Locate and identify every blood parasite.
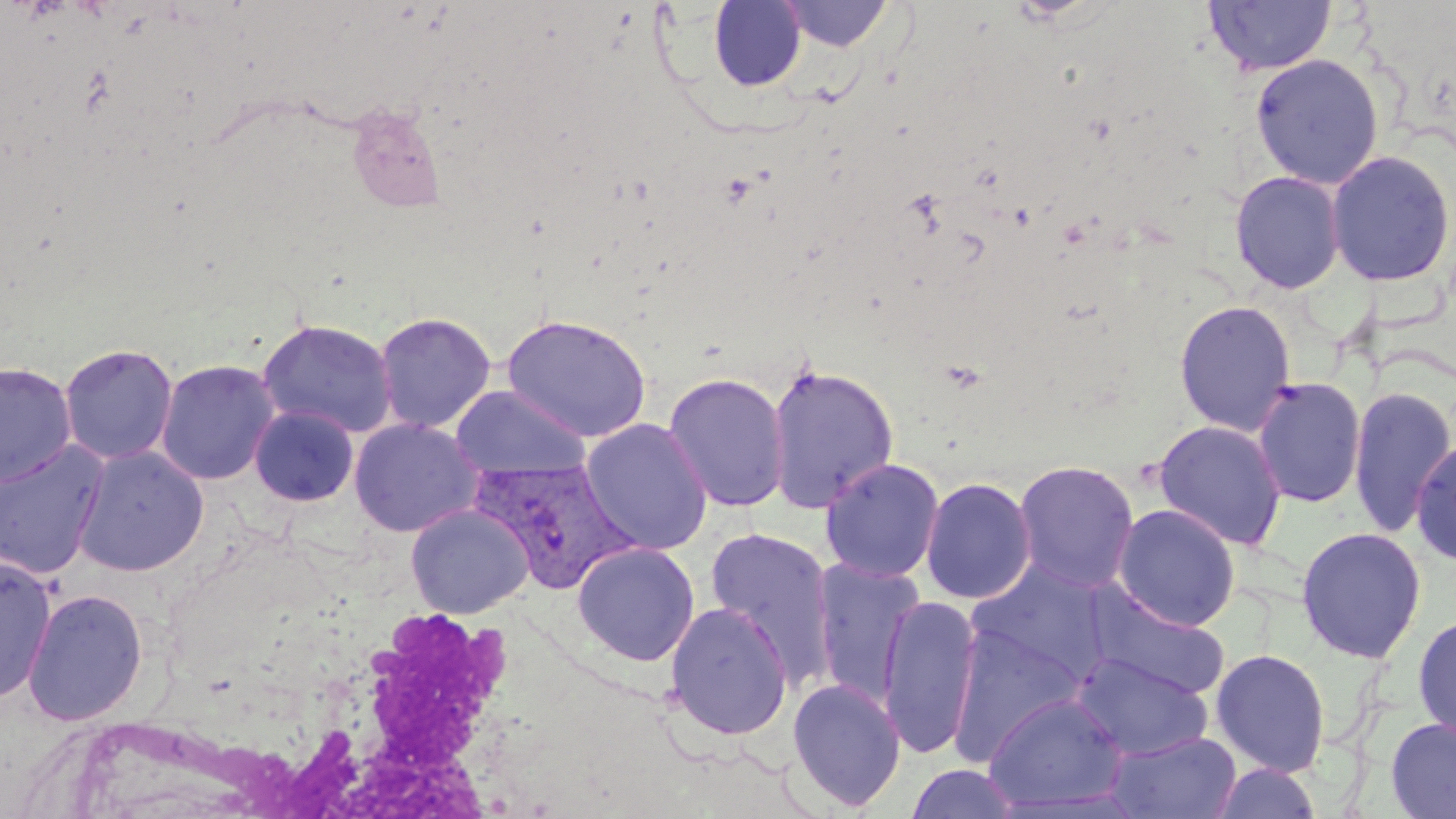

Approximate bounding boxes as (x1, y1, x2, y2) in pixels.
Plasmodium vivax-infected red blood cells: (469, 457, 639, 595).
No Plasmodium falciparum, Plasmodium ovale, Plasmodium malariae, Babesia divergens, or Trypanosoma brucei observed.

Summary:
  - Uninfected red blood cell locations: (1204, 0, 1336, 77), (709, 1, 806, 91), (779, 1, 894, 52), (1250, 53, 1385, 189), (346, 104, 447, 215), (1325, 149, 1455, 288), (1229, 170, 1346, 294), (1174, 300, 1296, 436), (374, 311, 496, 433), (501, 313, 652, 441), (257, 318, 398, 438), (59, 343, 178, 466), (156, 359, 281, 485), (0, 361, 76, 487), (764, 362, 899, 513), (663, 372, 791, 512), (1252, 376, 1366, 508), (450, 385, 592, 481), (1348, 385, 1456, 538), (249, 405, 360, 507), (580, 417, 713, 556), (348, 418, 485, 537), (1152, 419, 1288, 551), (1411, 438, 1456, 566), (0, 440, 110, 579), (72, 445, 209, 576), (819, 457, 944, 582), (1012, 459, 1140, 593), (920, 476, 1036, 604), (1112, 503, 1241, 631), (405, 504, 534, 618), (1295, 526, 1427, 663), (704, 527, 838, 686), (572, 541, 700, 665), (0, 555, 58, 702), (812, 559, 924, 707), (966, 559, 1112, 687), (1084, 585, 1231, 699), (22, 588, 149, 726), (878, 593, 982, 760), (665, 602, 793, 739), (1413, 614, 1456, 743), (946, 622, 1088, 762), (1210, 648, 1331, 777), (1072, 653, 1213, 760), (786, 677, 906, 812), (982, 691, 1130, 812), (1385, 717, 1456, 818), (1106, 730, 1242, 818), (1206, 761, 1323, 819), (906, 764, 1021, 819)
  - White blood cell locations: (282, 598, 530, 808)
  - Slide-level diagnosis: Plasmodium vivax
  - Field of view: single
  - Preparation: thin blood smear
  - Modality: light microscopy
  - Magnification: 1000x
  - Image size: 1456×819 pixels
  - Stain: May-Grünwald-Giemsa